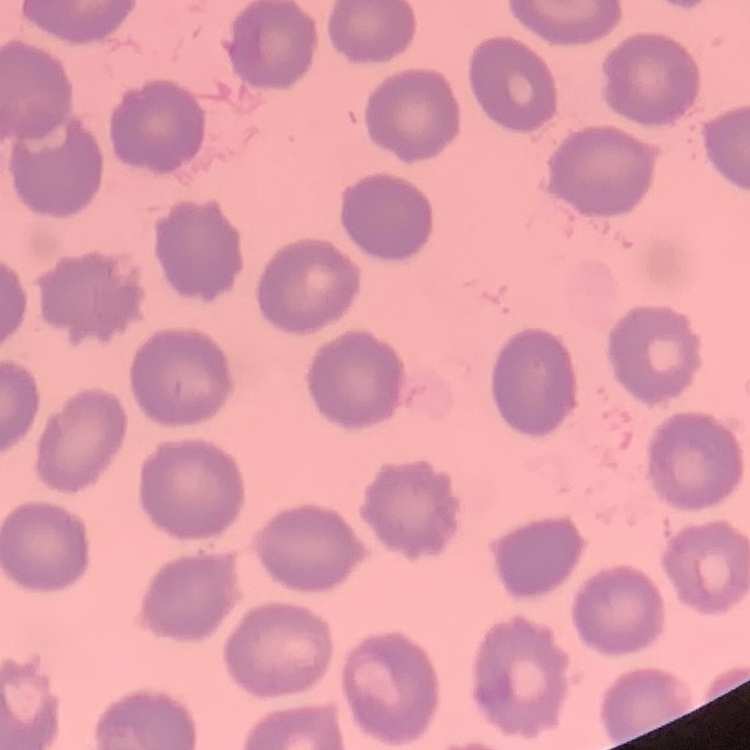 The red blood cells exhibit no rouleaux formation. One tile cut from a larger photomicrograph. Stained with either Field's or Giemsa. Thin peripheral smear.